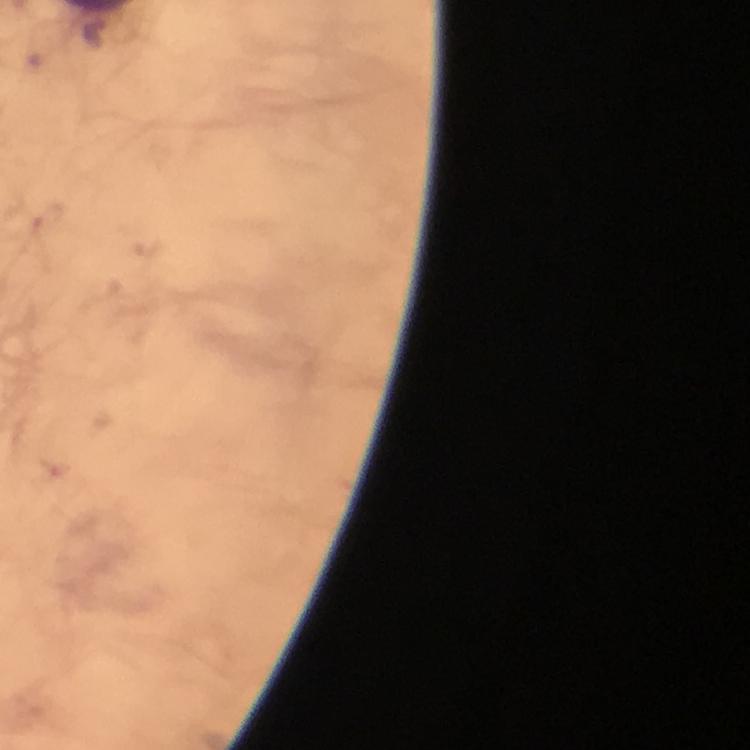

Approximate centers as [x, y] in pixels. Plasmodium parasite locations: [49, 218]. Thick blood film. A crop from one field of view. Immersion oil was used. 100x magnification. Photographed with a smartphone mounted on the microscope. From a diagnostic examination for malaria. Giemsa stain. Image is 750×750 pixels.